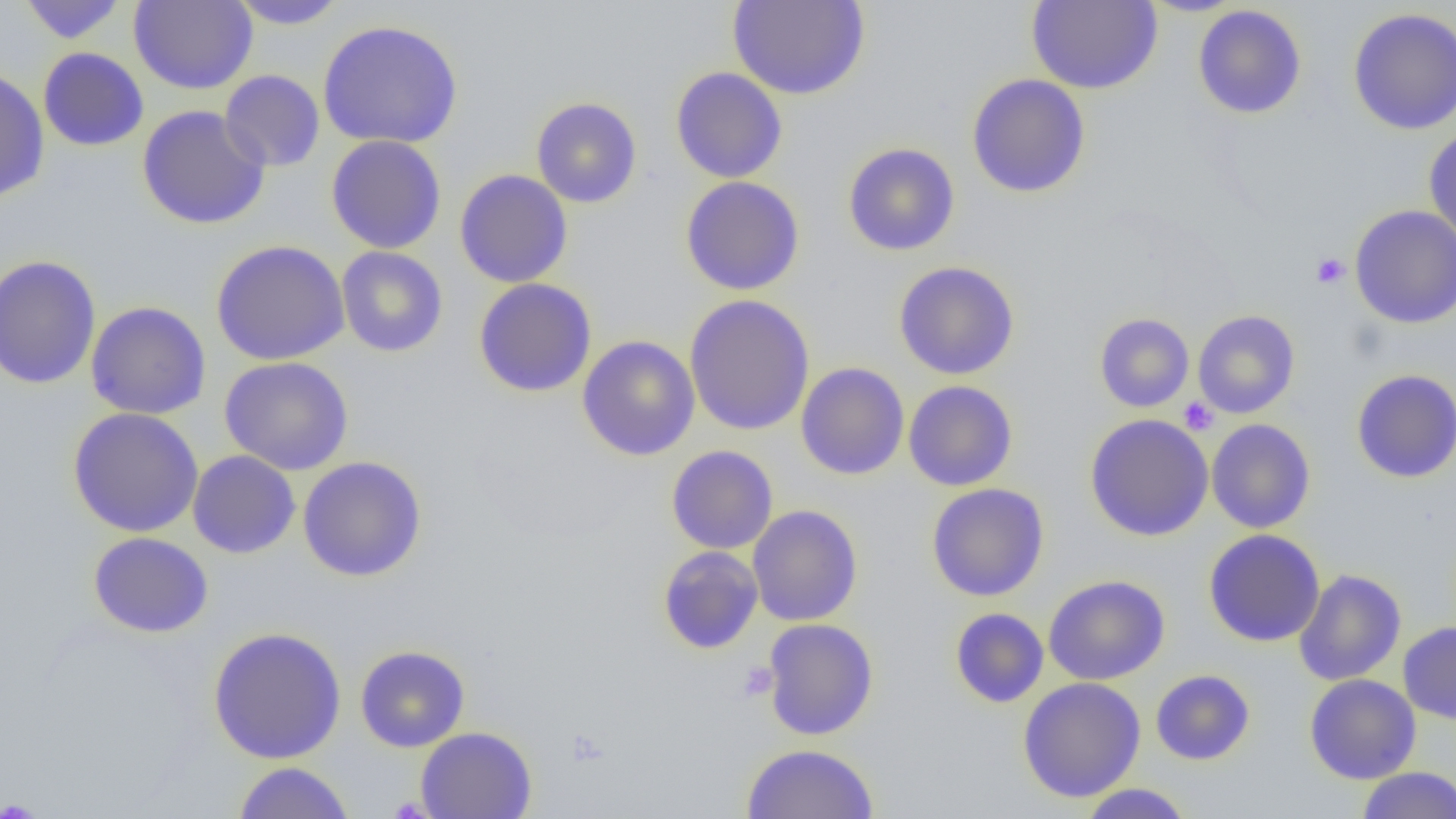
Approximate bounding boxes as named x1/y1/x2/y2 corners in pixels. Uninfected red blood cell locations: (x1=18, y1=0, x2=128, y2=44), (x1=129, y1=0, x2=258, y2=94), (x1=728, y1=0, x2=870, y2=100), (x1=1027, y1=0, x2=1162, y2=94), (x1=228, y1=1, x2=348, y2=29), (x1=1193, y1=5, x2=1307, y2=119), (x1=1348, y1=7, x2=1456, y2=135), (x1=318, y1=19, x2=464, y2=149), (x1=38, y1=47, x2=149, y2=151), (x1=0, y1=67, x2=50, y2=203), (x1=670, y1=67, x2=788, y2=183), (x1=220, y1=70, x2=325, y2=172), (x1=966, y1=73, x2=1090, y2=199), (x1=531, y1=97, x2=642, y2=208), (x1=137, y1=105, x2=270, y2=230), (x1=1423, y1=128, x2=1456, y2=244), (x1=325, y1=135, x2=446, y2=253), (x1=842, y1=142, x2=960, y2=256), (x1=454, y1=169, x2=573, y2=288), (x1=680, y1=176, x2=805, y2=296), (x1=1349, y1=204, x2=1456, y2=328), (x1=211, y1=239, x2=349, y2=365), (x1=336, y1=246, x2=448, y2=357), (x1=0, y1=255, x2=101, y2=390), (x1=893, y1=261, x2=1020, y2=380), (x1=473, y1=278, x2=597, y2=397), (x1=683, y1=294, x2=815, y2=436), (x1=86, y1=301, x2=211, y2=420), (x1=1192, y1=310, x2=1300, y2=418), (x1=1094, y1=312, x2=1194, y2=412), (x1=577, y1=335, x2=701, y2=461), (x1=219, y1=356, x2=354, y2=475), (x1=795, y1=362, x2=909, y2=480), (x1=1351, y1=369, x2=1456, y2=483), (x1=903, y1=380, x2=1018, y2=491), (x1=67, y1=408, x2=204, y2=537), (x1=1084, y1=414, x2=1214, y2=541), (x1=1206, y1=418, x2=1316, y2=533), (x1=666, y1=445, x2=778, y2=554), (x1=187, y1=451, x2=301, y2=559), (x1=298, y1=456, x2=427, y2=581), (x1=926, y1=483, x2=1049, y2=602), (x1=747, y1=505, x2=863, y2=626), (x1=1203, y1=529, x2=1325, y2=647), (x1=87, y1=532, x2=214, y2=638), (x1=657, y1=545, x2=763, y2=654), (x1=1294, y1=569, x2=1406, y2=686), (x1=1043, y1=575, x2=1170, y2=685), (x1=949, y1=607, x2=1049, y2=709), (x1=762, y1=618, x2=878, y2=741), (x1=1398, y1=621, x2=1456, y2=724), (x1=207, y1=626, x2=347, y2=764), (x1=355, y1=645, x2=470, y2=752), (x1=1150, y1=669, x2=1255, y2=765), (x1=1304, y1=674, x2=1421, y2=784), (x1=1018, y1=677, x2=1146, y2=802), (x1=416, y1=726, x2=537, y2=819), (x1=741, y1=743, x2=879, y2=819), (x1=232, y1=761, x2=355, y2=818), (x1=1357, y1=767, x2=1456, y2=819), (x1=1077, y1=783, x2=1194, y2=818). Platelet locations: (x1=1311, y1=252, x2=1350, y2=288), (x1=1178, y1=397, x2=1219, y2=435), (x1=737, y1=661, x2=778, y2=701), (x1=0, y1=799, x2=46, y2=818). Slide-level diagnosis: no evidence of blood parasites. Thin blood film. Single field of view. Image is 1456×819 pixels. Light microscopy. Captured at 1000x magnification.